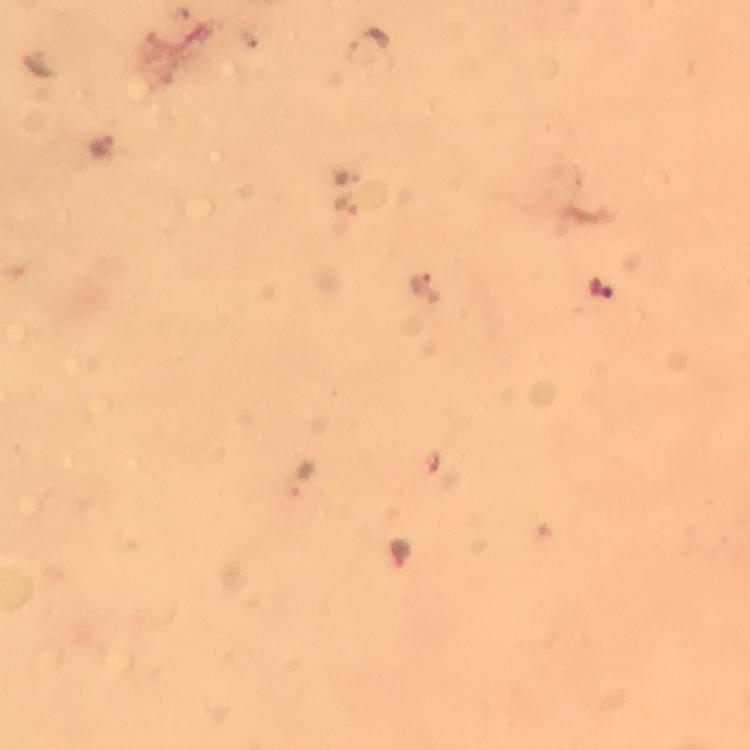
Approximate centers as (x, y) in pixels.
Summary:
  - Malaria parasite locations: (371, 41), (103, 143), (344, 175), (347, 209), (426, 284), (600, 292), (303, 480), (399, 551)
  - Immersion oil: used
  - Stain: Giemsa
  - Capture: smartphone mounted on the microscope
  - Context: from a malaria diagnostic workup
  - Image size: 750×750 pixels
  - Cropped from: a single field of view
  - Magnification: 100x
  - Preparation: thick blood film